Assess this cell for malaria.
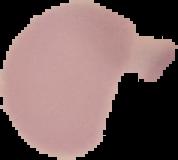

It is uninfected.

image size = 178×160 pixels
image type = segmented cell region with the area outside set to black
preparation = thin blood smear